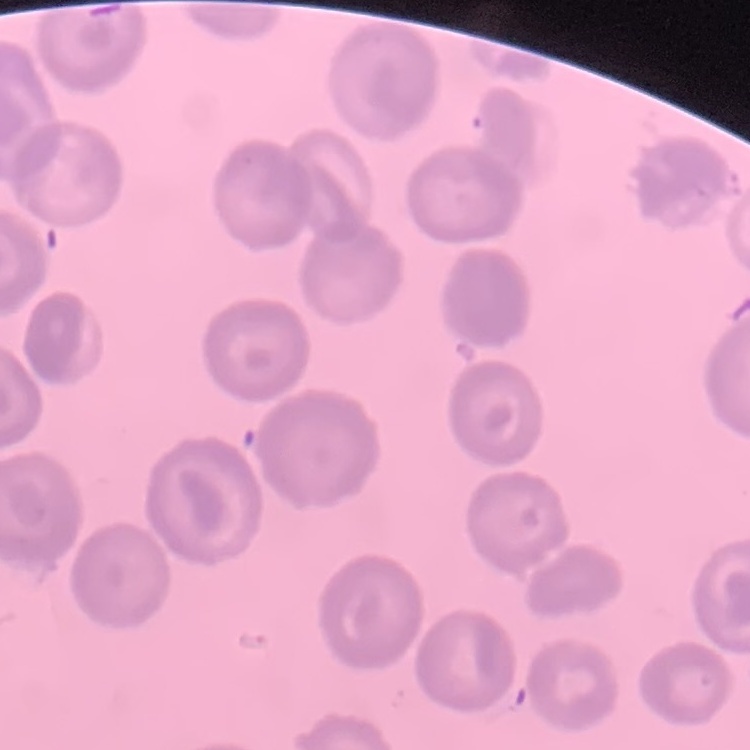

Summary:
  - Red blood cell morphology: no rouleaux formation
  - Stain: Field's or Giemsa
  - Preparation: thin blood smear
  - Image type: square crop of a larger photomicrograph